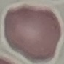
malaria status = uninfected
stain = Giemsa
preparation = thin blood film
image type = cell patch, automatically extracted from a larger field of view and resized to 64 × 64 pixels
capture = smartphone camera at the microscope eyepiece